Describe the morphology of the erythrocytes.
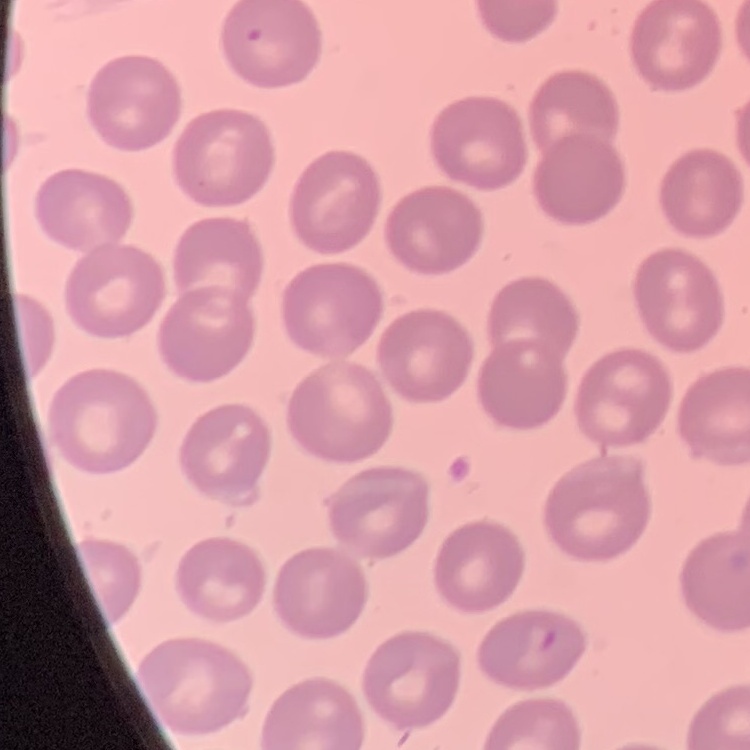
They show no rouleaux formation.

Square crop of a larger photomicrograph. Stained with either Field's or Giemsa. Thin blood film.